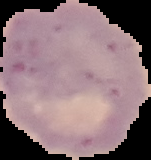
From a thin blood smear. The area outside the segmented cell region is set to black. Malaria status: uninfected. Image is 151×160 pixels.